Assess this cell for malaria.
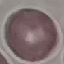
It is uninfected.

Summary:
  - Capture: smartphone through the microscope eyepiece
  - Preparation: thin blood film
  - Image type: automatically extracted cell patch, resized to 64 × 64 pixels
  - Stain: Giemsa